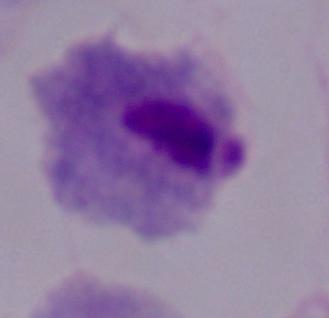

A trichomonad is seen. 1000x magnification. Micrograph.